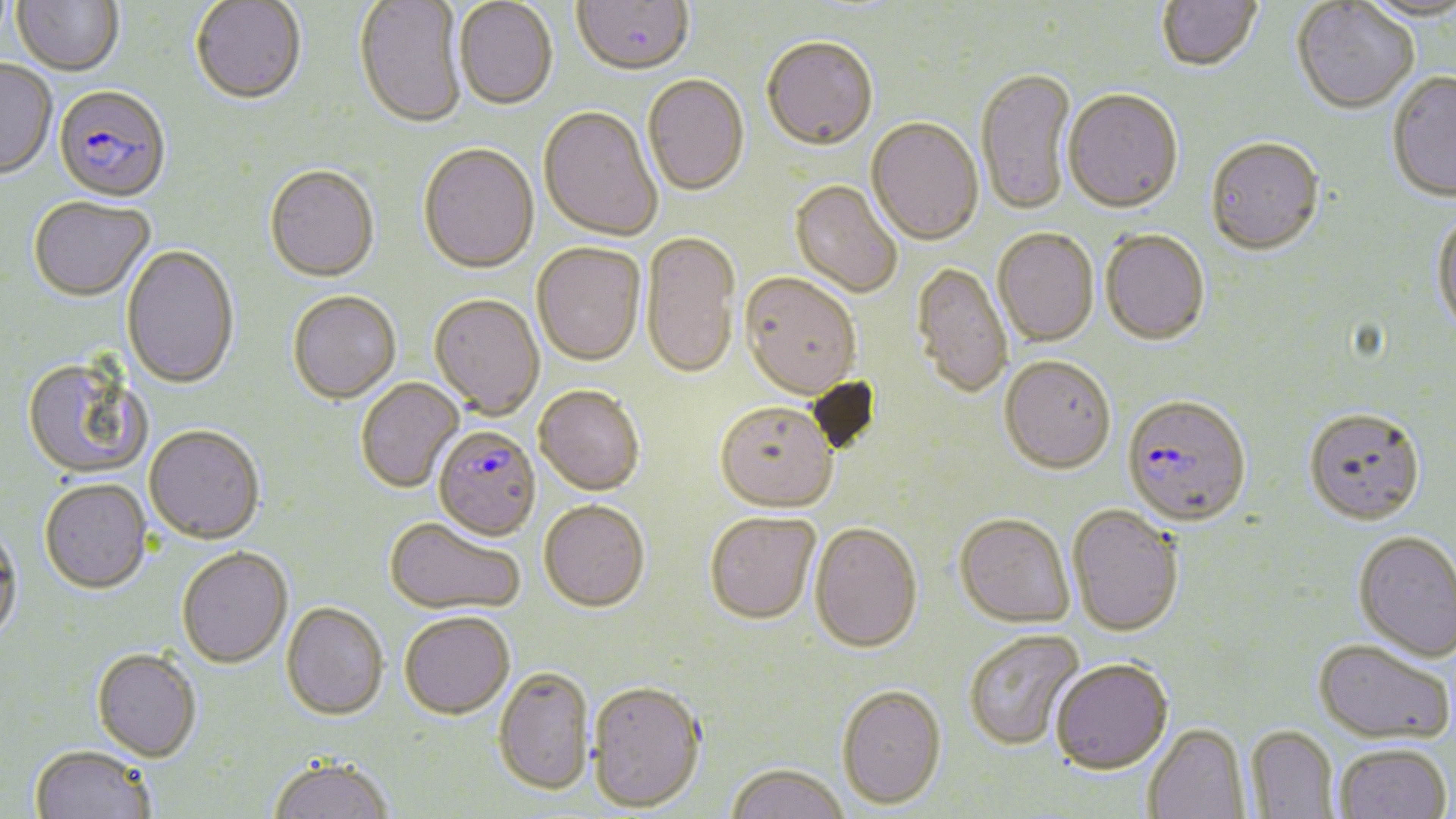
Summary:
  - Coordinate format: approximate bounding boxes as [x1, y1, x2, y2] in pixels
  - Uninfected red blood cell locations: [573, 0, 695, 75], [1156, 0, 1263, 74], [1356, 0, 1456, 23], [11, 1, 124, 77], [191, 1, 307, 105], [354, 1, 467, 130], [453, 1, 558, 111], [1292, 1, 1419, 114], [761, 35, 879, 151], [0, 59, 57, 180], [976, 67, 1076, 217], [1387, 71, 1456, 203], [643, 74, 750, 197], [1062, 88, 1184, 213], [538, 106, 663, 242], [866, 117, 984, 246], [1205, 137, 1324, 255], [418, 144, 539, 274], [264, 166, 380, 283], [790, 180, 903, 298], [28, 198, 155, 303], [1431, 210, 1456, 338], [993, 227, 1099, 347], [1100, 229, 1210, 345], [641, 231, 740, 380], [532, 242, 646, 366], [121, 245, 240, 391], [911, 263, 1013, 400], [740, 271, 862, 398], [288, 290, 401, 404], [429, 294, 545, 419], [999, 355, 1117, 474], [21, 358, 151, 481], [355, 378, 464, 493], [533, 384, 645, 495], [715, 400, 838, 512], [1304, 406, 1426, 524], [144, 425, 265, 544], [40, 479, 151, 595], [538, 499, 650, 612], [1067, 503, 1184, 636], [704, 511, 820, 624], [955, 512, 1075, 628], [384, 517, 524, 617], [810, 522, 922, 653], [0, 523, 23, 645], [1353, 530, 1456, 661], [177, 547, 293, 669], [280, 603, 389, 722], [399, 611, 515, 720], [963, 628, 1085, 751], [1314, 638, 1455, 744], [91, 648, 202, 763], [1050, 657, 1173, 773], [493, 666, 595, 797], [588, 680, 707, 812], [836, 684, 947, 809], [1142, 723, 1250, 819], [1246, 724, 1339, 818], [1334, 743, 1451, 819], [30, 746, 155, 819], [267, 757, 395, 819], [724, 762, 851, 819]
  - Plasmodium falciparum-infected red blood cell locations: [53, 86, 171, 204], [1122, 394, 1251, 525], [432, 424, 541, 541]
  - Slide-level diagnosis: Plasmodium falciparum
  - Field of view: single
  - Magnification: 1000x
  - Preparation: thin blood smear
  - Image size: 1456×819 pixels
  - Stain: May-Grünwald-Giemsa
  - Modality: light microscopy